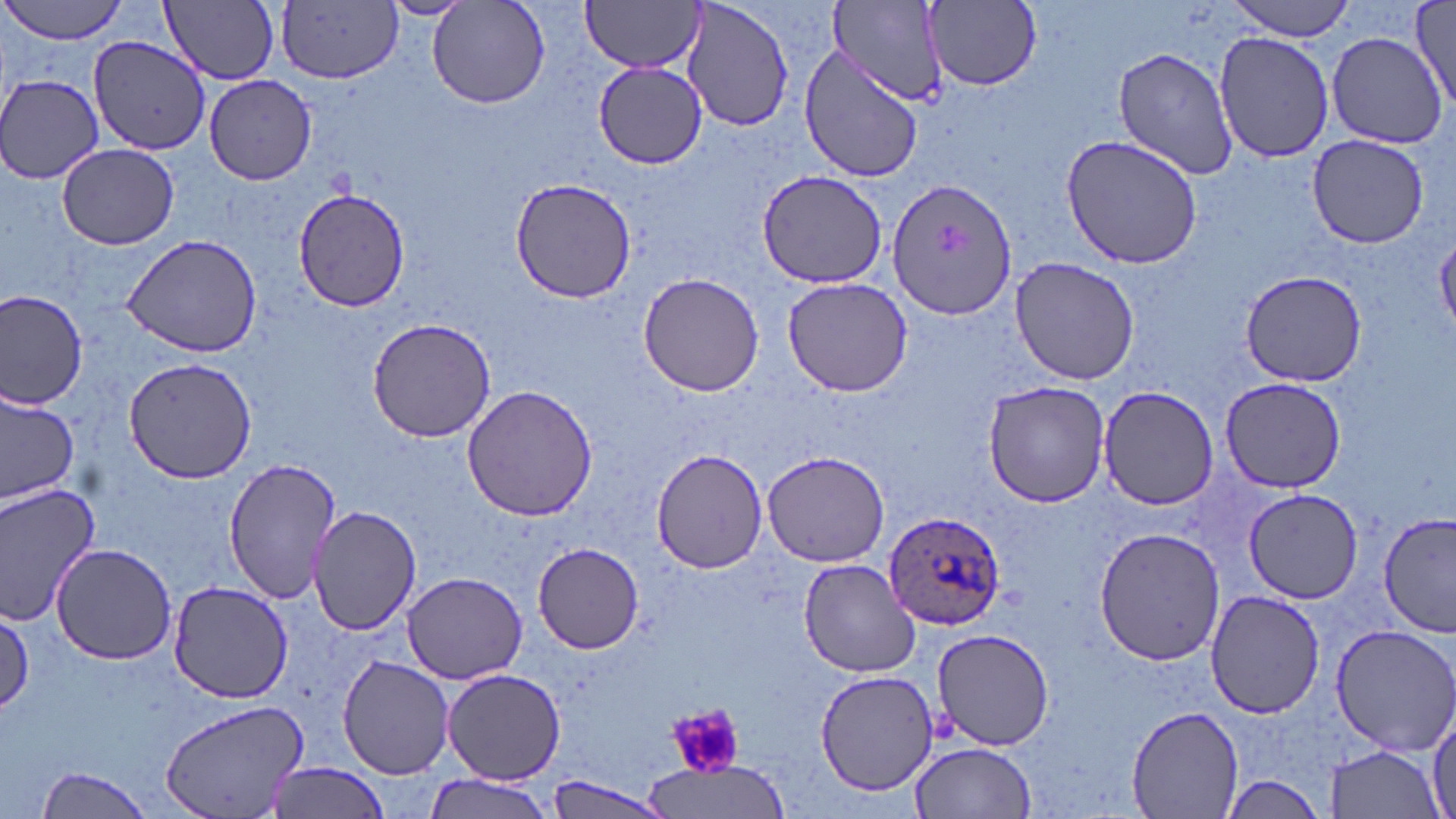 Approximate bounding boxes as [x1, y1, x2, y2] in pixels. Uninfected red blood cell locations: [3, 0, 128, 45], [162, 0, 279, 85], [827, 0, 950, 108], [921, 0, 1043, 94], [1226, 0, 1357, 40], [376, 1, 473, 21], [582, 1, 702, 75], [679, 1, 795, 135], [275, 2, 402, 84], [428, 2, 550, 109], [1411, 2, 1455, 111], [1213, 30, 1334, 164], [1324, 31, 1451, 148], [88, 36, 211, 156], [799, 46, 923, 185], [1114, 46, 1240, 179], [593, 63, 707, 168], [0, 74, 106, 183], [205, 74, 317, 185], [1061, 133, 1206, 269], [1307, 135, 1429, 247], [57, 143, 180, 250], [757, 171, 888, 288], [509, 177, 634, 302], [888, 180, 1019, 321], [294, 188, 410, 314], [119, 230, 264, 358], [1010, 257, 1140, 386], [1239, 268, 1367, 387], [636, 272, 767, 396], [781, 277, 914, 396], [0, 289, 90, 408], [367, 318, 496, 443], [121, 355, 259, 483], [1218, 375, 1349, 494], [981, 379, 1112, 508], [461, 385, 598, 523], [1099, 387, 1219, 508], [0, 389, 79, 506], [650, 448, 770, 575], [761, 451, 892, 568], [224, 458, 339, 604], [0, 483, 101, 623], [1242, 488, 1363, 604], [307, 505, 423, 633], [1377, 514, 1454, 639], [1093, 528, 1224, 667], [533, 542, 645, 653], [52, 543, 177, 664], [798, 559, 924, 677], [402, 572, 527, 683], [167, 579, 295, 703], [1205, 591, 1324, 719], [0, 606, 32, 714], [1327, 624, 1456, 756], [931, 627, 1058, 751], [338, 655, 453, 779], [443, 668, 565, 783], [813, 671, 940, 794], [161, 700, 310, 818], [1429, 704, 1456, 819], [1126, 705, 1247, 819], [911, 741, 1036, 819], [1323, 746, 1446, 817], [264, 760, 393, 819], [644, 762, 791, 819], [33, 765, 155, 819], [422, 774, 555, 818], [543, 776, 676, 818], [1216, 776, 1330, 816]. Platelet locations: [667, 703, 744, 780]. Plasmodium ovale-infected red blood cell locations: [883, 509, 1006, 630]. Slide-level diagnosis: Plasmodium ovale. 1000x magnification. May-Grünwald-Giemsa stain. Thin blood film. Light microscopy. One field of a larger specimen. Image is 1456×819 pixels.